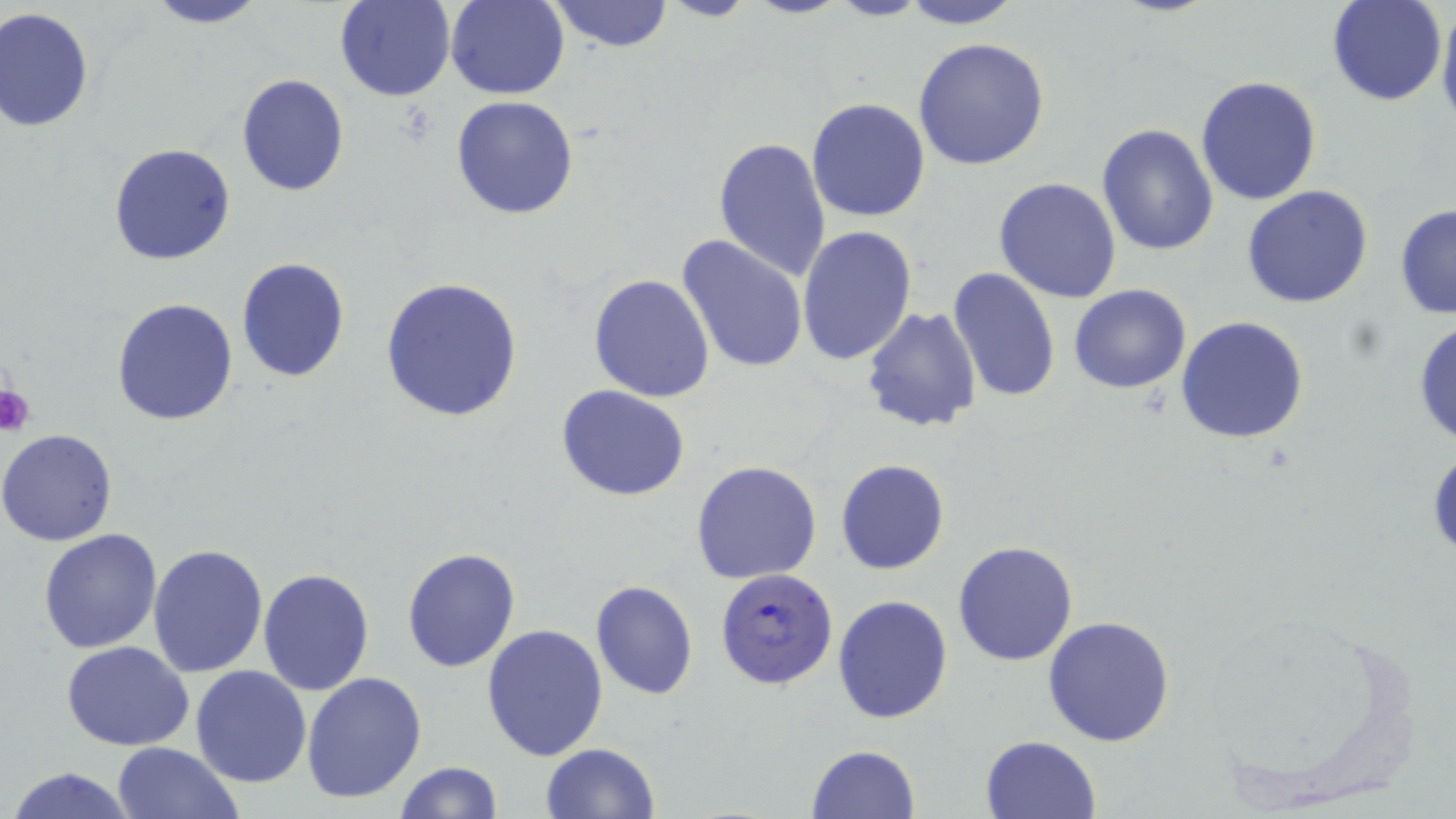
Approximate bounding boxes as named x1/y1/x2/y2 corners in pixels. Plasmodium falciparum-infected red blood cell locations: (x1=715, y1=566, x2=839, y2=692). Platelet locations: (x1=0, y1=382, x2=34, y2=437). Uninfected red blood cell locations: (x1=140, y1=0, x2=271, y2=28), (x1=334, y1=0, x2=455, y2=102), (x1=444, y1=0, x2=569, y2=99), (x1=549, y1=0, x2=675, y2=52), (x1=657, y1=0, x2=757, y2=22), (x1=898, y1=0, x2=1026, y2=28), (x1=1437, y1=0, x2=1456, y2=130), (x1=1325, y1=1, x2=1447, y2=106), (x1=1, y1=7, x2=95, y2=131), (x1=913, y1=37, x2=1051, y2=173), (x1=235, y1=73, x2=349, y2=196), (x1=1196, y1=75, x2=1324, y2=207), (x1=450, y1=95, x2=579, y2=221), (x1=806, y1=98, x2=931, y2=223), (x1=1097, y1=123, x2=1220, y2=255), (x1=712, y1=136, x2=833, y2=282), (x1=108, y1=143, x2=236, y2=265), (x1=994, y1=177, x2=1123, y2=303), (x1=1241, y1=185, x2=1374, y2=308), (x1=1394, y1=202, x2=1456, y2=321), (x1=798, y1=225, x2=918, y2=367), (x1=678, y1=234, x2=808, y2=375), (x1=235, y1=256, x2=351, y2=382), (x1=947, y1=268, x2=1061, y2=404), (x1=587, y1=273, x2=715, y2=402), (x1=379, y1=276, x2=523, y2=421), (x1=1068, y1=284, x2=1192, y2=395), (x1=109, y1=298, x2=240, y2=425), (x1=860, y1=305, x2=983, y2=432), (x1=1176, y1=315, x2=1310, y2=444), (x1=1411, y1=317, x2=1456, y2=449), (x1=555, y1=383, x2=691, y2=502), (x1=0, y1=427, x2=120, y2=546), (x1=835, y1=459, x2=950, y2=575), (x1=690, y1=460, x2=823, y2=585), (x1=39, y1=528, x2=163, y2=653), (x1=952, y1=540, x2=1078, y2=666), (x1=149, y1=544, x2=270, y2=680), (x1=400, y1=547, x2=520, y2=673), (x1=258, y1=568, x2=375, y2=696), (x1=589, y1=579, x2=699, y2=700), (x1=832, y1=594, x2=955, y2=724), (x1=1043, y1=615, x2=1176, y2=747), (x1=480, y1=624, x2=609, y2=762), (x1=60, y1=640, x2=194, y2=751), (x1=190, y1=665, x2=311, y2=788), (x1=303, y1=671, x2=427, y2=804), (x1=980, y1=734, x2=1100, y2=818), (x1=110, y1=741, x2=242, y2=819), (x1=806, y1=742, x2=922, y2=818), (x1=540, y1=743, x2=659, y2=819), (x1=394, y1=761, x2=503, y2=818), (x1=8, y1=766, x2=138, y2=819). Slide-level diagnosis: Plasmodium falciparum. May-Grünwald-Giemsa stain. Light microscopy. Captured at 1000x magnification. Image is 1456×819 pixels. Thin blood smear. Single field of view.